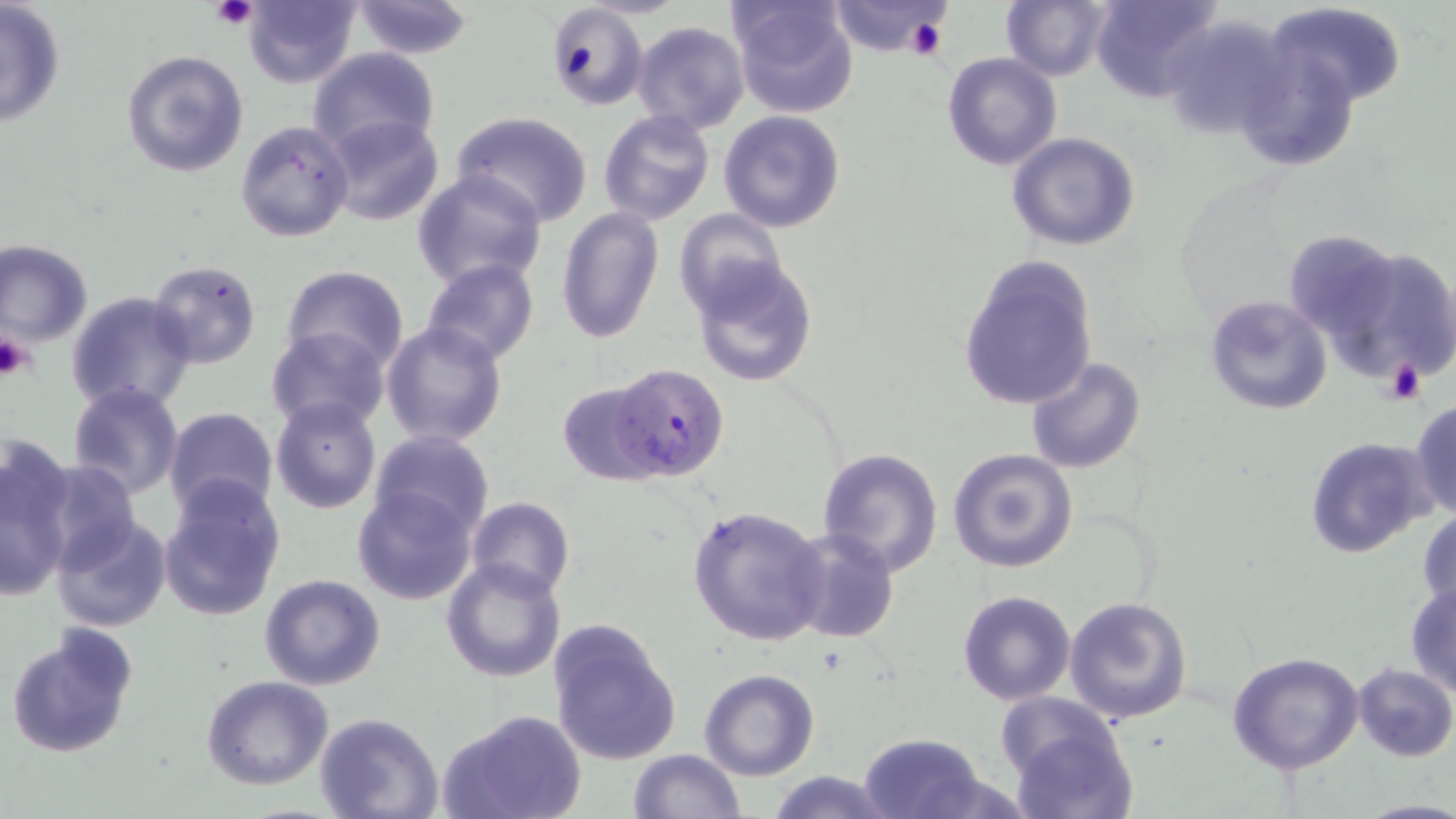

slide-level diagnosis = Plasmodium falciparum
magnification = 1000x
uninfected red blood cell locations = approximate bounding boxes as [x1, y1, x2, y2] in pixels: [1, 0, 68, 129], [242, 0, 363, 88], [349, 0, 477, 60], [728, 0, 860, 119], [1001, 0, 1111, 81], [1090, 0, 1225, 105], [831, 1, 956, 59], [1267, 2, 1406, 106], [544, 4, 649, 111], [1162, 16, 1293, 139], [629, 21, 750, 135], [1233, 43, 1364, 172], [306, 47, 441, 161], [120, 48, 250, 178], [942, 51, 1064, 171], [598, 110, 715, 226], [719, 110, 846, 233], [451, 112, 593, 227], [323, 114, 446, 228], [235, 118, 356, 243], [1007, 131, 1140, 251], [411, 169, 549, 292], [673, 207, 787, 318], [554, 208, 663, 344], [1283, 229, 1402, 340], [1, 240, 94, 348], [1321, 244, 1456, 387], [955, 253, 1099, 412], [689, 257, 819, 387], [421, 258, 541, 367], [147, 259, 262, 370], [281, 262, 408, 373], [66, 290, 197, 415], [1204, 293, 1334, 416], [381, 321, 509, 449], [265, 327, 391, 435], [1025, 356, 1147, 475], [556, 379, 669, 487], [67, 382, 183, 499], [271, 396, 382, 514], [1409, 399, 1456, 520], [164, 407, 280, 519], [368, 430, 495, 542], [1304, 435, 1436, 559], [0, 447, 76, 594], [817, 447, 945, 576], [947, 448, 1079, 574], [36, 459, 142, 572], [158, 476, 287, 622], [353, 485, 477, 606], [465, 496, 575, 601], [687, 503, 829, 647], [1417, 510, 1456, 615], [50, 512, 172, 632], [788, 530, 899, 643], [441, 558, 566, 682], [259, 574, 387, 692], [1405, 580, 1456, 696], [957, 590, 1076, 705], [1064, 595, 1193, 725], [546, 620, 682, 766], [5, 624, 138, 761], [1227, 650, 1366, 774], [1353, 663, 1456, 761], [699, 669, 820, 780], [202, 676, 332, 790], [998, 701, 1132, 815], [442, 709, 587, 819], [315, 712, 443, 819], [859, 732, 987, 819], [628, 748, 745, 818], [764, 770, 894, 819], [1357, 798, 1456, 818]
modality = light microscopy
platelet locations = approximate bounding boxes as [x1, y1, x2, y2] in pixels: [211, 0, 257, 30], [905, 17, 949, 61], [0, 330, 39, 380], [1386, 358, 1425, 406]
Plasmodium falciparum-infected red blood cell locations = approximate bounding boxes as [x1, y1, x2, y2] in pixels: [613, 362, 728, 479]
stain = May-Grünwald-Giemsa
preparation = thin blood smear
field of view = one of a larger specimen
image size = 1456×819 pixels